Locate and identify every blood parasite.
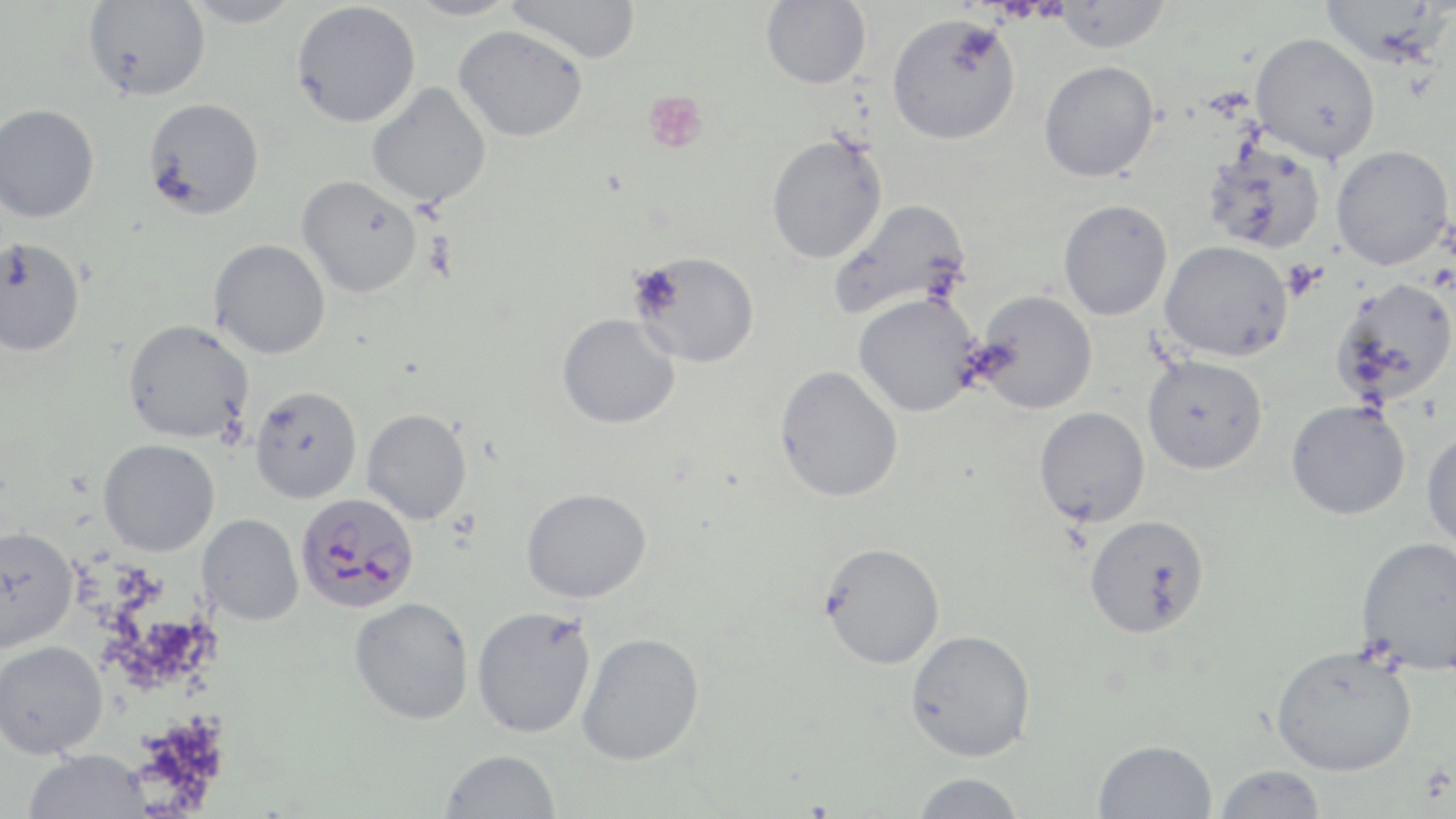
Approximate bounding boxes as (x1, y1, x2, y2) in pixels.
Plasmodium falciparum-infected red blood cells: (295, 493, 419, 613).
No Plasmodium ovale, Plasmodium malariae, Plasmodium vivax, Babesia divergens, or Trypanosoma brucei observed.

slide-level diagnosis = Plasmodium falciparum
uninfected red blood cell locations = approximate bounding boxes as (x1, y1, x2, y2) in pixels: (182, 0, 303, 28), (403, 0, 521, 20), (505, 0, 642, 64), (761, 0, 871, 89), (1320, 0, 1448, 66), (82, 1, 211, 102), (291, 1, 421, 128), (1052, 1, 1171, 53), (886, 13, 1021, 145), (454, 25, 587, 141), (1250, 31, 1380, 162), (1038, 60, 1159, 182), (367, 82, 491, 208), (143, 98, 264, 220), (0, 103, 100, 224), (765, 133, 888, 264), (1203, 140, 1327, 255), (1331, 145, 1453, 270), (297, 176, 422, 298), (829, 198, 971, 321), (1058, 199, 1173, 321), (0, 237, 85, 357), (209, 239, 331, 359), (1159, 240, 1294, 361), (629, 250, 759, 368), (1331, 277, 1456, 409), (973, 289, 1098, 414), (853, 293, 980, 417), (557, 313, 680, 429), (122, 319, 254, 444), (1142, 354, 1268, 474), (775, 365, 903, 502), (250, 386, 362, 503), (1286, 400, 1410, 520), (1033, 406, 1150, 527), (361, 409, 472, 524), (1421, 428, 1456, 553), (98, 438, 219, 556), (521, 486, 653, 604), (198, 514, 303, 625), (1084, 514, 1210, 638), (0, 524, 78, 652), (1355, 536, 1456, 676), (819, 542, 945, 669), (350, 597, 474, 725), (471, 606, 597, 738), (905, 629, 1036, 761), (576, 632, 705, 765), (0, 640, 108, 758), (1270, 644, 1417, 776), (1093, 739, 1217, 819), (24, 748, 150, 818), (440, 749, 561, 819), (1213, 764, 1327, 819), (910, 772, 1026, 819)
stain = May-Grünwald-Giemsa
field of view = single
image size = 1456×819 pixels
platelet locations = approximate bounding boxes as (x1, y1, x2, y2) in pixels: (641, 89, 709, 154)
modality = light microscopy
preparation = thin blood smear
magnification = 1000x